Classify this cell by malaria status.
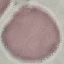
Uninfected.

stain = Giemsa
preparation = thin blood film
capture = smartphone through the microscope eyepiece
image type = automatically extracted cell patch, resized to 64 × 64 pixels